Describe the morphology of the red blood cells.
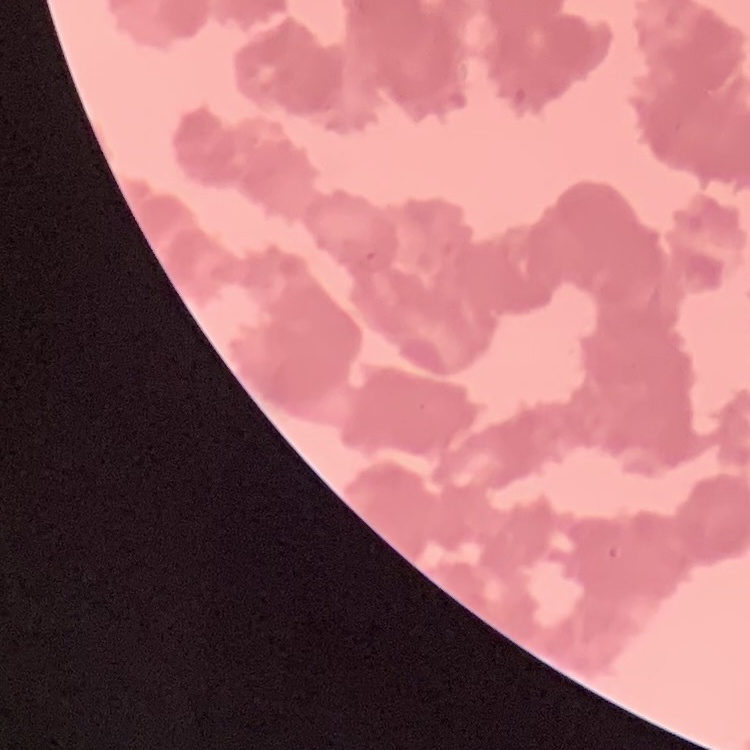
They show rouleaux formation.

preparation = thin blood smear
image type = one tile cut from a larger photomicrograph
stain = Field's or Giemsa